Locate every malaria parasite.
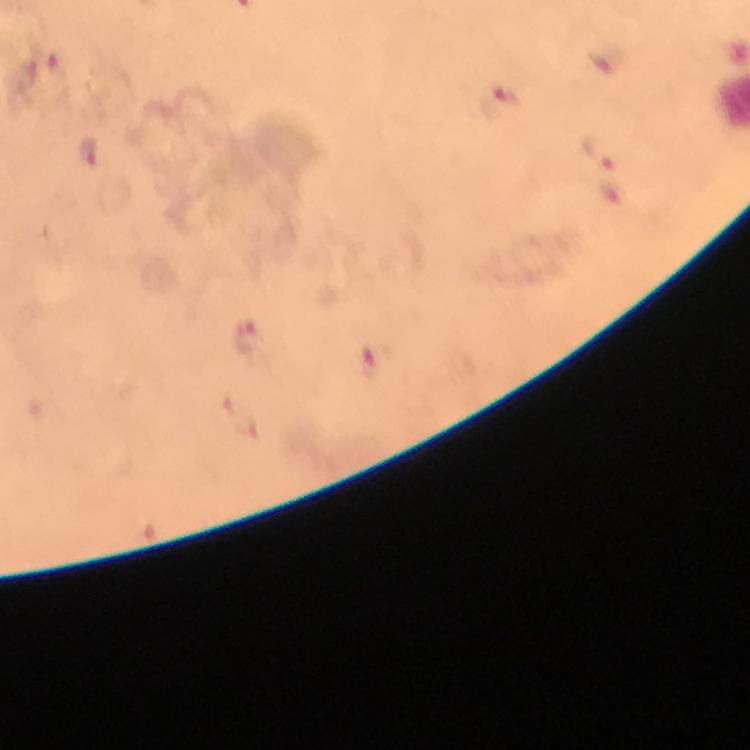

Approximate object centers, in pixels from the top-left corner.
Malaria parasites: (x=608, y=58), (x=499, y=102), (x=602, y=151), (x=89, y=155), (x=246, y=338), (x=371, y=362).

Photographed through the microscope with a smartphone camera. Thick blood film. Immersion oil was used. From a malaria diagnostic workup. At 100x magnification. Giemsa-stained preparation. Cropped region of a single field of view. Image is 750×750 pixels.